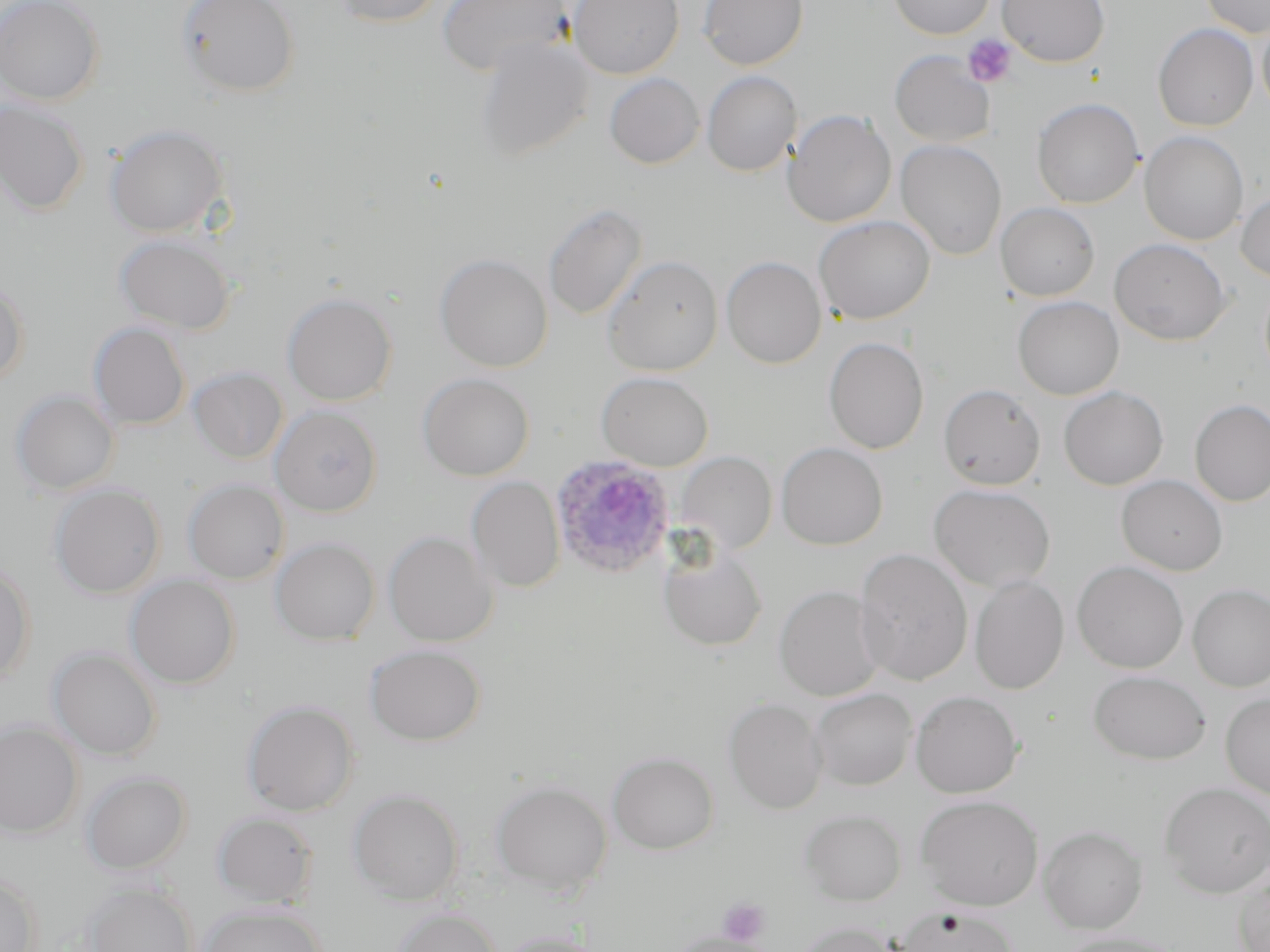

slide-level diagnosis = Plasmodium ovale
uninfected red blood cell locations = approximate bounding boxes as [x1, y1, x2, y2] in pixels: [0, 0, 104, 105], [176, 0, 300, 98], [332, 0, 445, 27], [436, 0, 571, 76], [568, 0, 684, 79], [698, 0, 808, 69], [889, 0, 994, 39], [997, 0, 1110, 66], [1199, 0, 1270, 38], [1257, 16, 1270, 118], [1153, 23, 1258, 132], [475, 38, 594, 162], [889, 50, 995, 147], [701, 71, 802, 176], [604, 73, 705, 168], [1032, 98, 1143, 209], [0, 99, 89, 215], [783, 109, 896, 228], [105, 123, 230, 238], [1139, 131, 1249, 245], [895, 139, 1007, 260], [1236, 189, 1270, 283], [1002, 201, 1111, 397], [543, 202, 647, 321], [996, 202, 1099, 301], [813, 215, 935, 324], [114, 233, 237, 335], [1109, 238, 1231, 345], [434, 253, 553, 372], [602, 254, 723, 376], [722, 256, 826, 369], [0, 280, 29, 389], [282, 292, 397, 406], [1013, 296, 1123, 400], [88, 322, 190, 430], [824, 336, 929, 454], [188, 367, 288, 464], [596, 371, 713, 471], [418, 373, 534, 481], [938, 383, 1045, 490], [1059, 386, 1168, 490], [11, 389, 119, 496], [1189, 399, 1270, 506], [270, 406, 382, 517], [776, 442, 888, 550], [676, 452, 777, 555], [1116, 475, 1228, 575], [467, 476, 565, 593], [183, 479, 289, 584], [49, 484, 165, 599], [928, 484, 1056, 592], [384, 530, 497, 647], [271, 537, 380, 645], [658, 544, 768, 651], [853, 548, 973, 686], [0, 561, 35, 686], [1072, 561, 1188, 673], [126, 575, 240, 689], [969, 575, 1069, 694], [1188, 584, 1270, 691], [774, 585, 884, 702], [365, 644, 485, 746], [48, 646, 162, 761], [1088, 670, 1211, 764], [809, 688, 916, 790], [910, 690, 1023, 798], [1221, 693, 1270, 799], [724, 697, 826, 814], [242, 700, 359, 816], [0, 721, 84, 838], [607, 752, 719, 854], [81, 770, 192, 874], [490, 780, 612, 895], [1159, 782, 1270, 898], [348, 788, 464, 905], [915, 795, 1043, 910], [800, 808, 906, 905], [211, 811, 318, 908], [1039, 825, 1148, 933], [1232, 867, 1270, 952], [0, 871, 41, 952], [82, 882, 198, 952], [711, 899, 775, 947], [198, 904, 327, 952], [895, 907, 1020, 952], [394, 908, 502, 952], [793, 920, 900, 952], [497, 930, 608, 952], [1055, 931, 1187, 952], [668, 933, 773, 952]
field of view = single
platelet locations = approximate bounding boxes as [x1, y1, x2, y2] in pixels: [962, 34, 1016, 88], [717, 897, 770, 946]
preparation = thin blood smear
stain = May-Grünwald-Giemsa
modality = light microscopy
magnification = 1000x
Plasmodium ovale-infected red blood cell locations = approximate bounding boxes as [x1, y1, x2, y2] in pixels: [551, 457, 674, 578]
image size = 1270×952 pixels